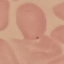

Summary:
  - Malaria status: uninfected
  - Image type: automatically extracted cell patch, resized to 64 × 64 pixels
  - Preparation: thin blood smear
  - Stain: Giemsa
  - Capture: smartphone through the microscope eyepiece